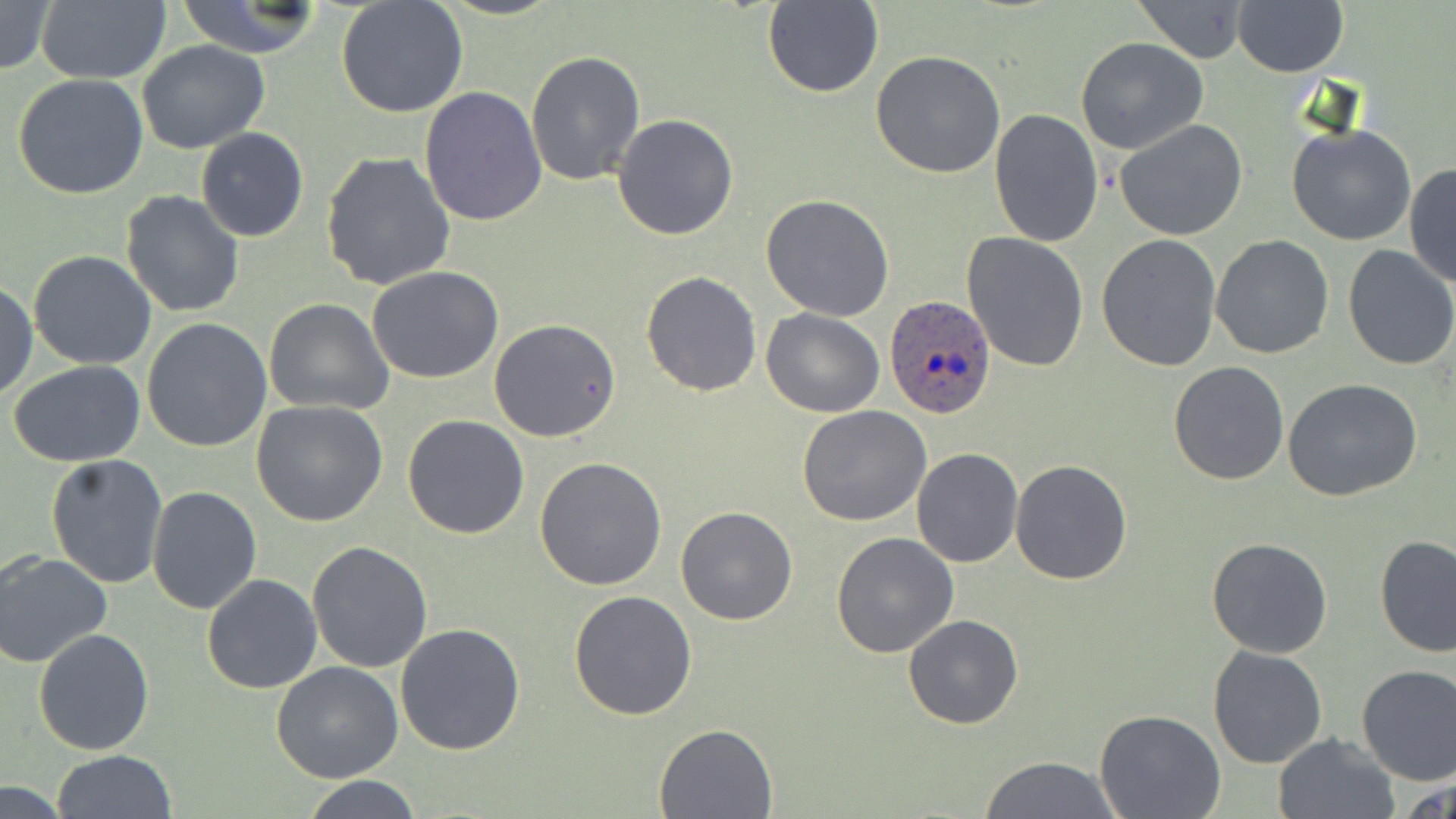
slide-level diagnosis = Plasmodium ovale
preparation = thin blood smear
stain = May-Grünwald-Giemsa
image size = 1456×819 pixels
magnification = 1000x
modality = light microscopy
field of view = single
uninfected red blood cell locations = approximate bounding boxes as (x1,y1)-(x2,y2) corner pairs in pixels: (35,0)-(170,84), (1131,0)-(1255,62), (1231,0)-(1347,76), (0,1)-(55,76), (174,2)-(330,58), (335,2)-(469,120), (762,2)-(885,98), (1076,37)-(1207,154), (136,40)-(270,154), (871,50)-(1005,178), (524,51)-(646,186), (12,73)-(150,199), (420,87)-(548,228), (989,108)-(1104,248), (612,113)-(741,241), (1114,119)-(1248,241), (1285,123)-(1417,247), (195,127)-(308,242), (320,151)-(457,291), (1404,161)-(1456,290), (120,190)-(246,318), (760,194)-(895,321), (961,232)-(1090,374), (1096,234)-(1222,372), (1209,235)-(1334,359), (1341,245)-(1456,369), (28,249)-(158,369), (367,267)-(505,384), (641,270)-(763,396), (0,282)-(37,400), (264,298)-(394,416), (761,308)-(886,417), (142,318)-(274,453), (489,319)-(622,442), (8,359)-(148,467), (1169,361)-(1290,484), (1284,378)-(1423,500), (250,400)-(389,526), (797,406)-(932,527), (403,413)-(529,540), (912,448)-(1024,567), (44,455)-(168,589), (535,455)-(668,591), (1009,458)-(1135,585), (147,485)-(263,615), (676,506)-(799,625), (830,531)-(960,659), (1375,535)-(1455,659), (1205,537)-(1334,659), (307,540)-(433,672), (0,550)-(112,669), (202,574)-(323,693), (568,591)-(697,721), (903,613)-(1025,729), (396,623)-(527,756), (33,628)-(156,755), (1208,645)-(1327,769), (272,662)-(404,784), (1355,663)-(1456,784), (1093,710)-(1224,818), (655,722)-(777,818), (1272,733)-(1398,818), (51,750)-(179,819), (977,756)-(1125,818), (1400,775)-(1454,819), (299,776)-(424,817), (0,782)-(75,817)
Plasmodium ovale-infected red blood cell locations = approximate bounding boxes as (x1,y1)-(x2,y2) corner pairs in pixels: (882,294)-(996,419)